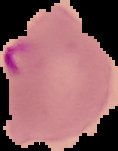
Summary:
  - Image type: cell region segmented out of the field of view; surrounding area masked to black
  - Result: Plasmodium parasites detected
  - Image size: 118×151 pixels
  - Preparation: thin blood smear